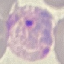

Result: malaria parasites identified. Cell patch, automatically extracted from a larger field of view and resized to 64 × 64 pixels. Photographed with a smartphone camera at the microscope eyepiece. Giemsa-stained preparation. Thin blood smear.